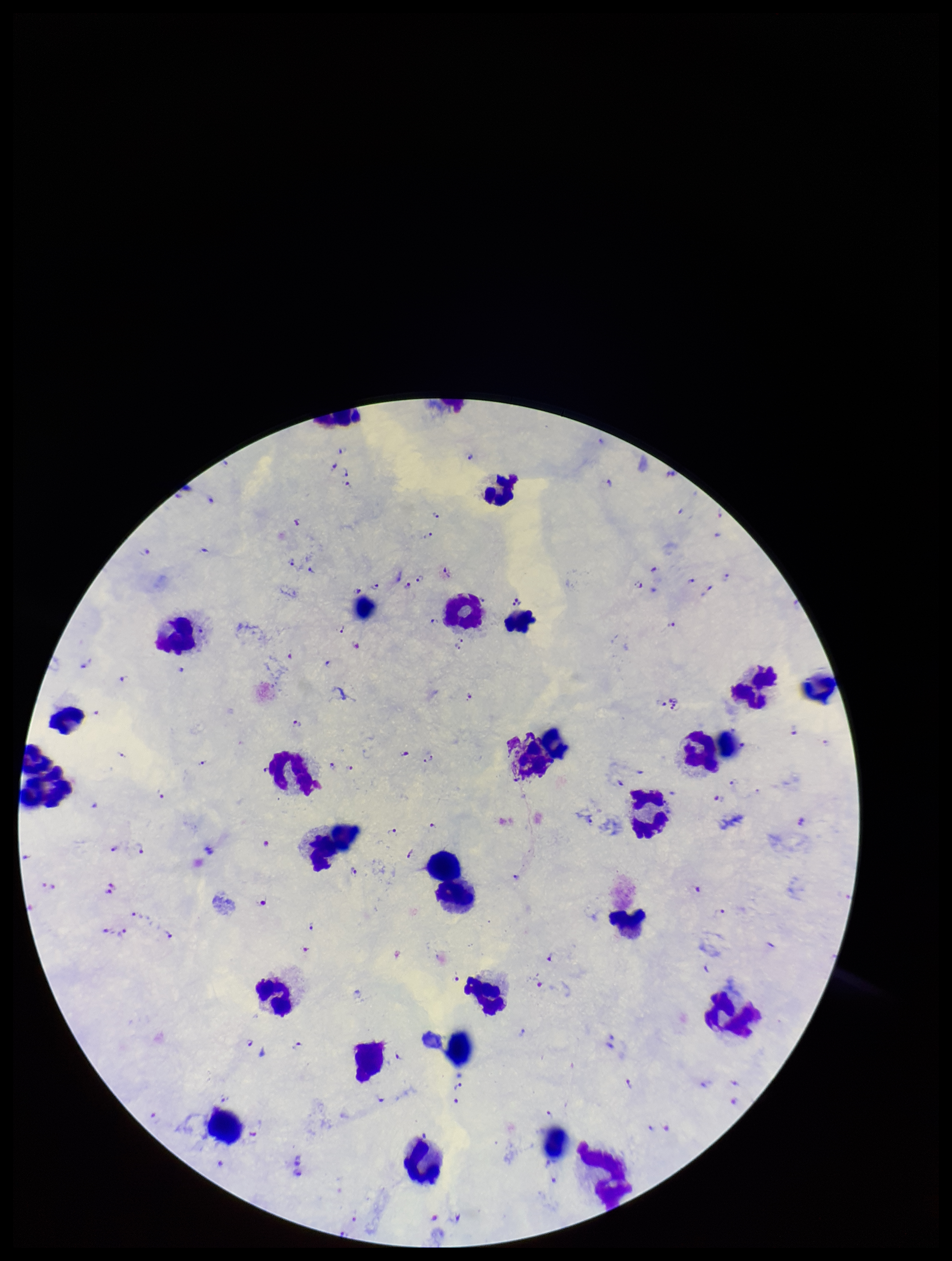
Leukocyte count: 27. Parasite count: 104. Giemsa stain. Image is 952×1261 pixels. Photographed through the microscope eyepiece with a smartphone camera. Patient malaria status: positive. Species reported for this patient: Plasmodium falciparum. Preparation: thick smear. Plasmodium parasites: detected. One field from this slide.